Locate every leukocyte (white blood cell).
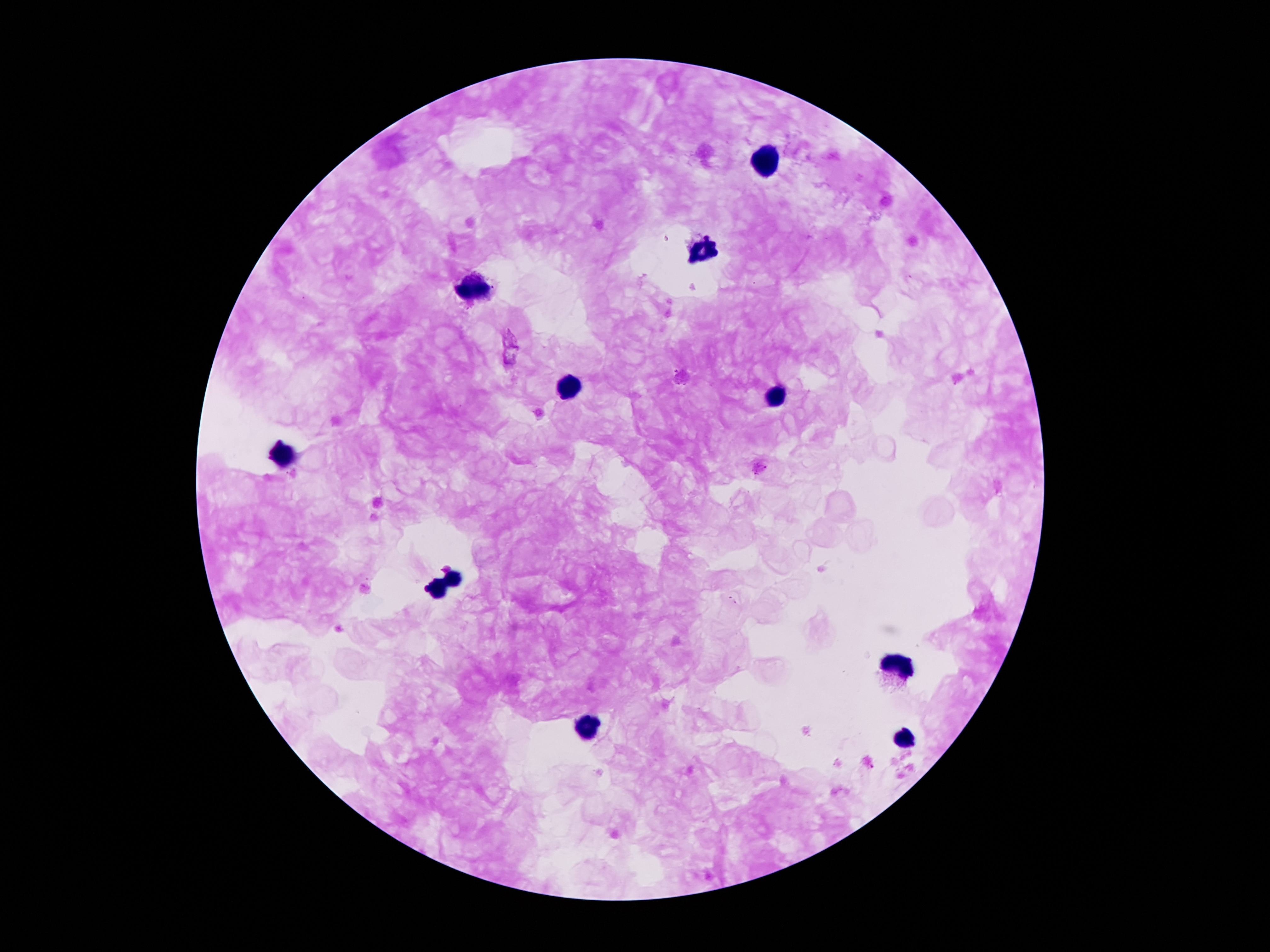
Approximate centers as {x, y} in pixels.
Leukocytes: {768, 162}, {699, 253}, {477, 289}, {569, 390}, {776, 400}, {286, 452}, {454, 578}, {436, 587}, {895, 665}, {587, 728}, {906, 741}.

Plasmodium parasite locations = {733, 600}
patient malaria status = positive for Plasmodium falciparum
field of view = single
preparation = thick peripheral-blood smear
magnification = 100x
stain = Giemsa
image size = 1270×952 pixels
capture = smartphone through the microscope eyepiece